Locate every blood parasite and identify its species.
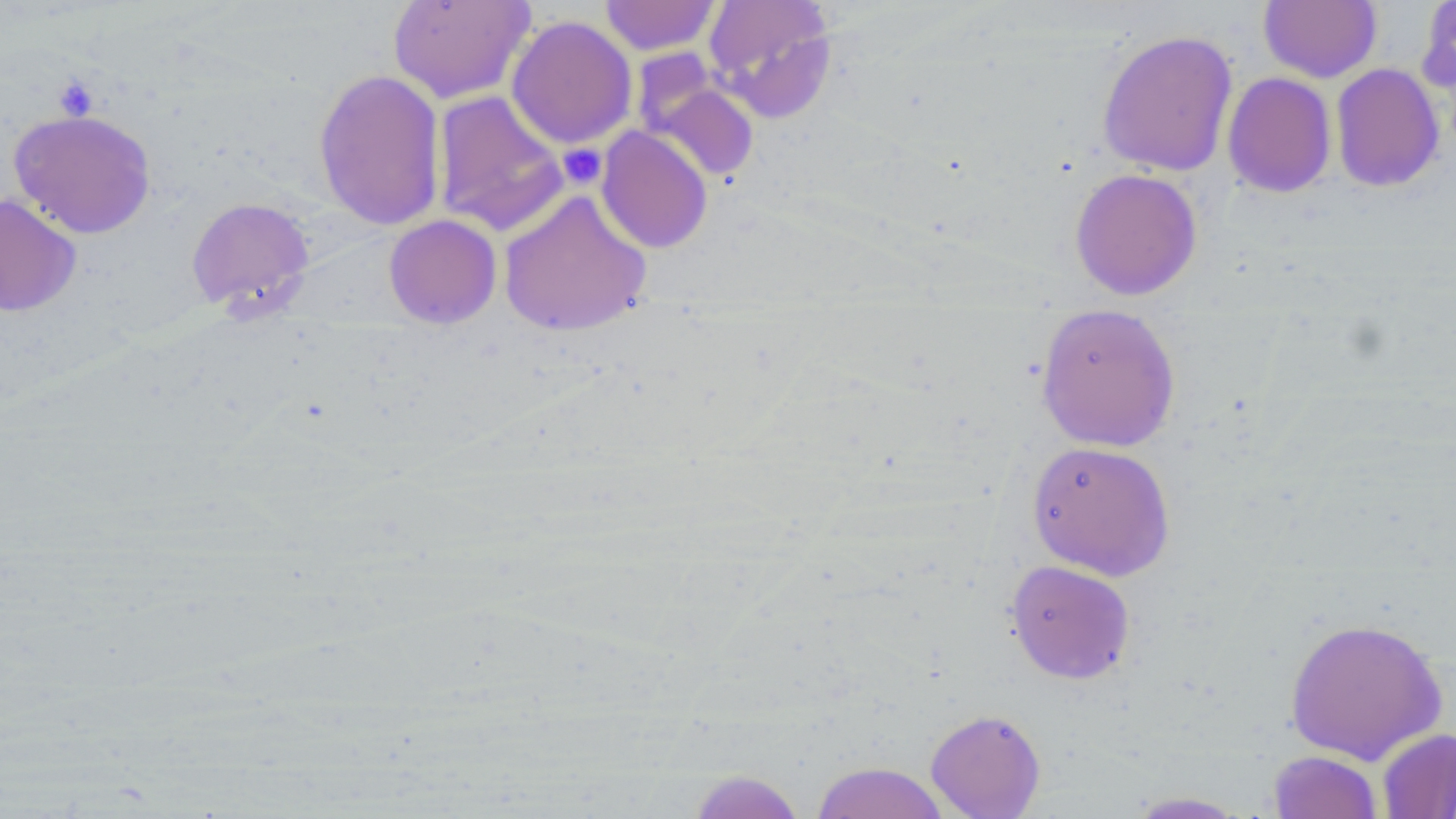

No blood parasites observed.

Summary:
  - Coordinate format: approximate bounding boxes as named x1/y1/x2/y2 corners in pixels
  - Uninfected red blood cell locations: (x1=386, y1=0, x2=534, y2=104), (x1=599, y1=0, x2=722, y2=56), (x1=703, y1=0, x2=838, y2=121), (x1=1259, y1=1, x2=1382, y2=83), (x1=1417, y1=1, x2=1456, y2=97), (x1=506, y1=15, x2=637, y2=150), (x1=1096, y1=29, x2=1238, y2=176), (x1=1330, y1=63, x2=1445, y2=192), (x1=313, y1=67, x2=446, y2=231), (x1=641, y1=71, x2=760, y2=183), (x1=1222, y1=72, x2=1337, y2=198), (x1=432, y1=90, x2=570, y2=237), (x1=8, y1=108, x2=157, y2=239), (x1=596, y1=125, x2=713, y2=254), (x1=1069, y1=168, x2=1203, y2=300), (x1=498, y1=189, x2=652, y2=337), (x1=0, y1=193, x2=81, y2=317), (x1=186, y1=197, x2=316, y2=317), (x1=384, y1=214, x2=502, y2=329), (x1=1035, y1=304, x2=1181, y2=452), (x1=1025, y1=440, x2=1176, y2=581), (x1=1004, y1=559, x2=1136, y2=685), (x1=1283, y1=616, x2=1448, y2=765), (x1=925, y1=708, x2=1046, y2=819), (x1=1377, y1=728, x2=1456, y2=818), (x1=1268, y1=750, x2=1383, y2=819), (x1=810, y1=761, x2=950, y2=819), (x1=686, y1=769, x2=807, y2=819), (x1=1122, y1=791, x2=1253, y2=818)
  - Platelet locations: (x1=53, y1=76, x2=99, y2=120), (x1=558, y1=143, x2=607, y2=190)
  - Slide-level diagnosis: negative for blood parasites
  - Magnification: 1000x
  - Preparation: thin blood film
  - Field of view: one of a larger specimen
  - Stain: May-Grünwald-Giemsa
  - Modality: optical microscopy
  - Image size: 1456×819 pixels